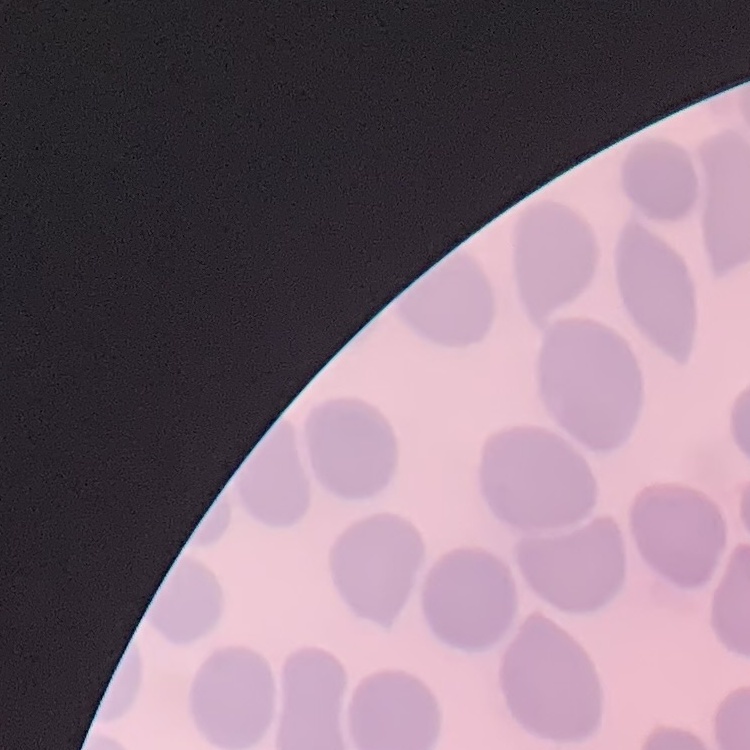

Summary:
  - Erythrocyte morphology: no rouleaux formation
  - Stain: Field's or Giemsa
  - Preparation: thin peripheral smear
  - Image type: one tile cut from a larger photomicrograph